Point out every Plasmodium parasite.
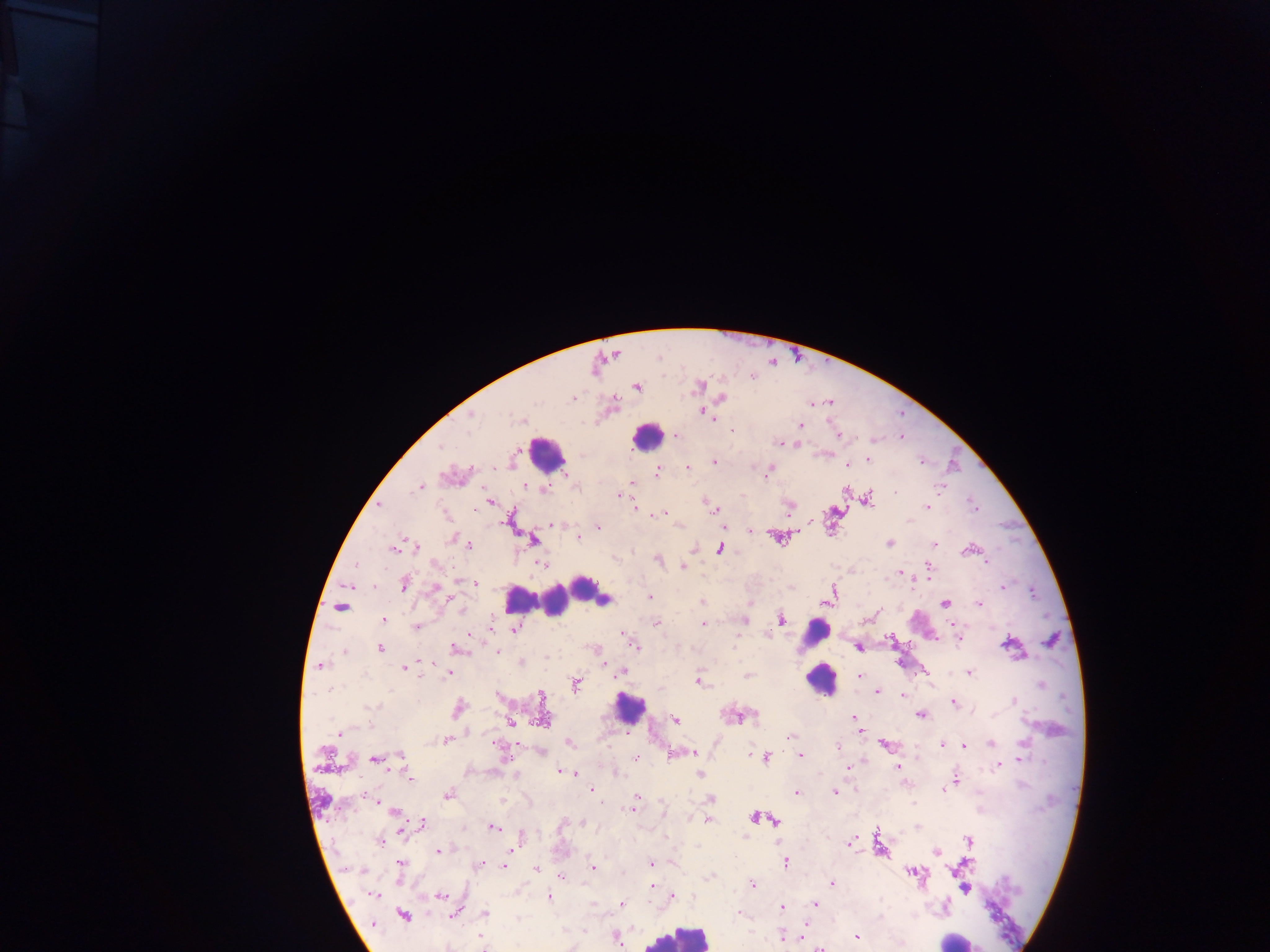
Approximate centers as [x, y] in pixels.
Plasmodium parasites: [700, 386], [637, 387], [572, 398], [722, 398], [830, 402], [811, 405], [703, 413], [472, 414], [712, 417], [523, 421], [800, 426], [733, 430], [677, 435], [839, 435], [779, 443], [795, 444], [868, 460], [714, 463], [847, 465], [687, 467], [657, 472], [768, 474], [632, 483], [526, 486], [547, 488], [939, 488], [418, 489], [896, 492], [620, 495], [867, 499], [490, 502], [927, 507], [974, 507], [713, 508], [660, 514], [552, 525], [598, 528], [751, 530], [578, 537], [453, 539], [534, 540], [890, 543], [467, 544], [934, 544], [414, 547], [394, 548], [720, 548], [966, 550], [658, 560], [987, 562], [541, 564], [355, 565], [436, 565], [683, 566], [928, 568], [899, 573], [475, 583], [404, 584], [1003, 587], [436, 588], [833, 589], [650, 596], [604, 599], [701, 602], [826, 603], [945, 603], [978, 603], [340, 608], [461, 609], [384, 619], [781, 619], [744, 621], [656, 624], [703, 624], [952, 624], [416, 627], [515, 629], [766, 634], [624, 636], [958, 637], [1008, 644], [635, 647], [858, 647], [380, 649], [457, 649], [344, 651], [497, 652], [520, 662], [321, 666], [404, 668], [622, 672], [448, 673], [969, 673], [747, 675], [860, 676], [699, 682], [577, 684], [331, 689], [877, 691], [903, 694], [542, 697], [1014, 701], [953, 703], [372, 706], [459, 708], [921, 716], [751, 717], [854, 718], [543, 720], [675, 720], [510, 722], [860, 730], [338, 732], [789, 737], [446, 740], [570, 743], [990, 743], [1023, 744], [885, 745], [942, 745], [965, 746], [837, 747], [498, 748], [542, 752], [685, 752], [401, 754], [694, 754], [675, 755], [800, 755], [636, 758], [765, 758], [1021, 759], [374, 760], [999, 764], [847, 767], [898, 767], [560, 771], [571, 772], [617, 775], [699, 775], [409, 777], [955, 779], [945, 789], [593, 792], [796, 792], [834, 793], [448, 795], [637, 798], [711, 799], [374, 800], [601, 802], [915, 803], [633, 809], [664, 809], [395, 812], [754, 817], [708, 820], [775, 821], [423, 823], [582, 823], [493, 827], [402, 829], [522, 837], [378, 840], [968, 841], [850, 842], [438, 850], [937, 852], [786, 863], [966, 863], [481, 864], [651, 864], [399, 865], [505, 865], [592, 867], [536, 869], [360, 871], [913, 873], [710, 875], [560, 876], [832, 883], [753, 885], [652, 887], [964, 889], [373, 895], [440, 895], [673, 895], [549, 898], [622, 903], [815, 903], [781, 907], [485, 914], [739, 914], [453, 915], [403, 916], [584, 932], [782, 935], [616, 937], [802, 937], [856, 937], [482, 943], [820, 948].

Leukocyte locations: [646, 437], [546, 454], [584, 587], [519, 599], [555, 601], [816, 633], [816, 654], [820, 680], [628, 709], [676, 936], [958, 939]. Image is 1270×952 pixels. Sample from Ghana. Thick blood film. One field of view. Photographed through a microscope with a mobile-phone camera.